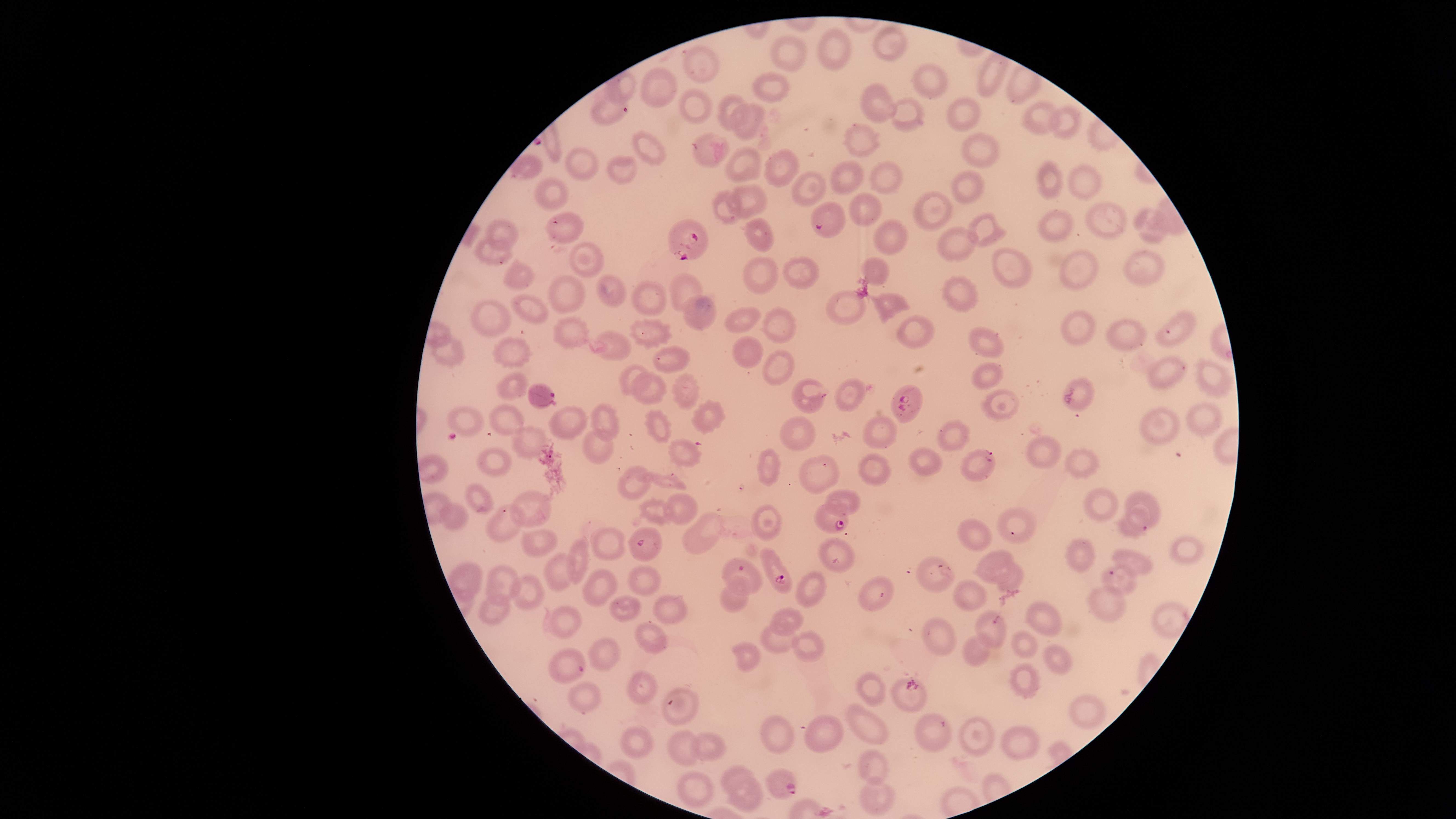

Approximate marker points as (x, y) in pixels.
Summary:
  - Parasitized red blood cells: (826, 220), (685, 242), (542, 394), (905, 406), (832, 519), (775, 569)
  - Uninfected red blood cells: (888, 46), (830, 48), (794, 59), (700, 63), (989, 80), (931, 82), (652, 83), (779, 85), (687, 101), (728, 103), (880, 104), (962, 107), (606, 108), (909, 114), (1060, 115), (1041, 118), (751, 122), (652, 144), (864, 146), (979, 146), (712, 147), (745, 163), (781, 163), (588, 164), (526, 166), (619, 168), (849, 176), (885, 178), (1038, 181), (1087, 181), (805, 187), (966, 187), (553, 195), (745, 198), (859, 205), (933, 207), (727, 209), (1105, 217), (558, 224), (506, 226), (1150, 226), (1049, 227), (983, 230), (765, 232), (894, 240), (956, 243), (493, 251), (593, 259), (1003, 262), (1082, 269), (1145, 269), (518, 271), (874, 272), (759, 275), (800, 275), (683, 282), (613, 290), (567, 291), (964, 291), (649, 294), (885, 304), (848, 305), (524, 307), (697, 309), (488, 314), (748, 319), (1184, 325), (649, 326), (776, 327), (1075, 330), (908, 331), (570, 332), (1130, 336), (978, 340), (615, 345), (509, 353), (449, 354), (743, 354), (671, 362), (783, 368), (633, 370), (1213, 376), (987, 377), (1173, 378), (509, 385), (686, 387), (645, 390), (851, 393), (814, 395), (1083, 397), (996, 402), (705, 413), (1196, 417), (466, 419), (1156, 419), (601, 420), (565, 422), (505, 423), (660, 423), (883, 429), (951, 432), (801, 433), (533, 440), (598, 443), (685, 452), (1045, 452), (1082, 460), (494, 462), (928, 465), (766, 466), (875, 469), (814, 470), (635, 482), (480, 495), (844, 498), (1144, 500), (528, 503), (1102, 503), (683, 505), (650, 510), (453, 515), (766, 518), (1132, 524), (501, 525), (1016, 526), (703, 530), (980, 535), (607, 541), (537, 543), (1183, 546), (583, 549), (650, 551), (1079, 553), (837, 555), (991, 555), (1129, 560), (556, 568), (935, 568), (747, 571), (1012, 577), (499, 578), (464, 579), (1120, 580), (642, 582), (807, 589), (733, 590), (602, 591), (875, 591), (971, 591), (526, 594), (1113, 599), (674, 610), (622, 613), (1042, 613), (497, 616), (790, 616), (1164, 619), (568, 622), (995, 622), (939, 634), (647, 635), (779, 641), (1024, 644), (974, 650), (810, 652), (1053, 654), (745, 655), (607, 656), (568, 668), (1026, 678), (637, 684), (872, 691), (905, 697), (586, 700), (677, 708), (1086, 708), (864, 727), (936, 734), (823, 736), (781, 738), (976, 740), (1023, 742), (640, 743), (710, 743), (679, 748), (872, 764), (736, 771), (779, 781), (692, 790), (879, 794), (751, 799)
  - Visible region: circular
  - Field of view: single
  - Preparation: thin blood smear
  - Species: Plasmodium falciparum
  - Capture: smartphone photograph through the microscope eyepiece
  - Stain: Giemsa
  - Presence: malaria parasites seen
  - Image size: 1456×819 pixels